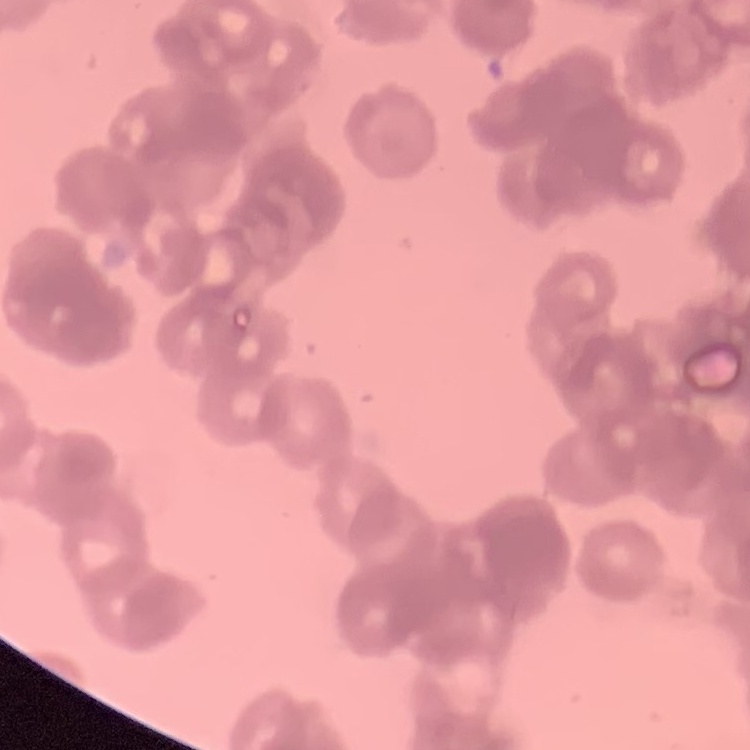

red blood cell morphology = rouleaux formation
preparation = thin blood film
image type = square crop of a larger photomicrograph
stain = Field's or Giemsa